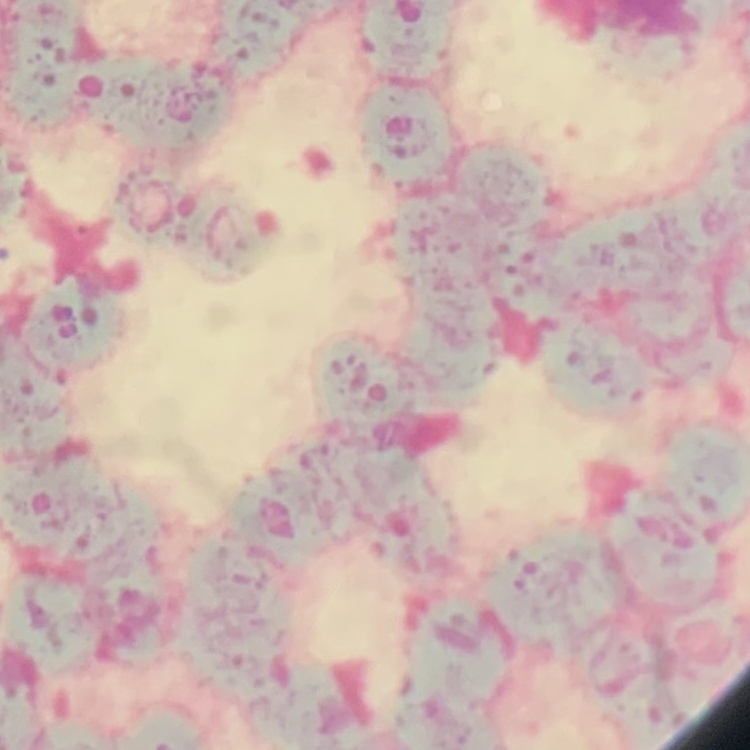
erythrocyte morphology = rouleaux formation
stain = Field's or Giemsa
preparation = thin blood smear
image type = one tile cut from a larger photomicrograph